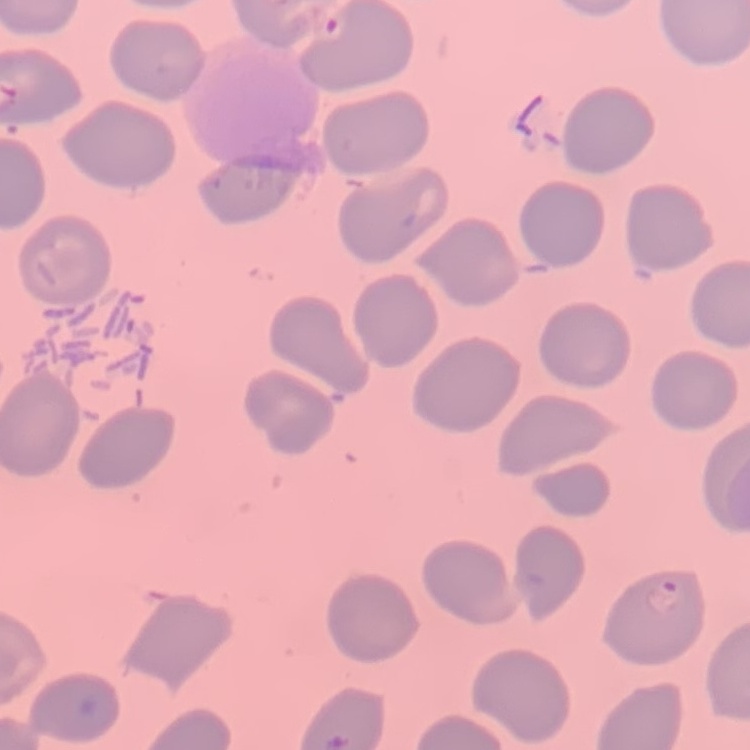
{
  "red_blood_cell_morphology": "no rouleaux formation",
  "stain": "Field's or Giemsa",
  "image_type": "square crop of a larger photomicrograph",
  "preparation": "thin blood smear"
}